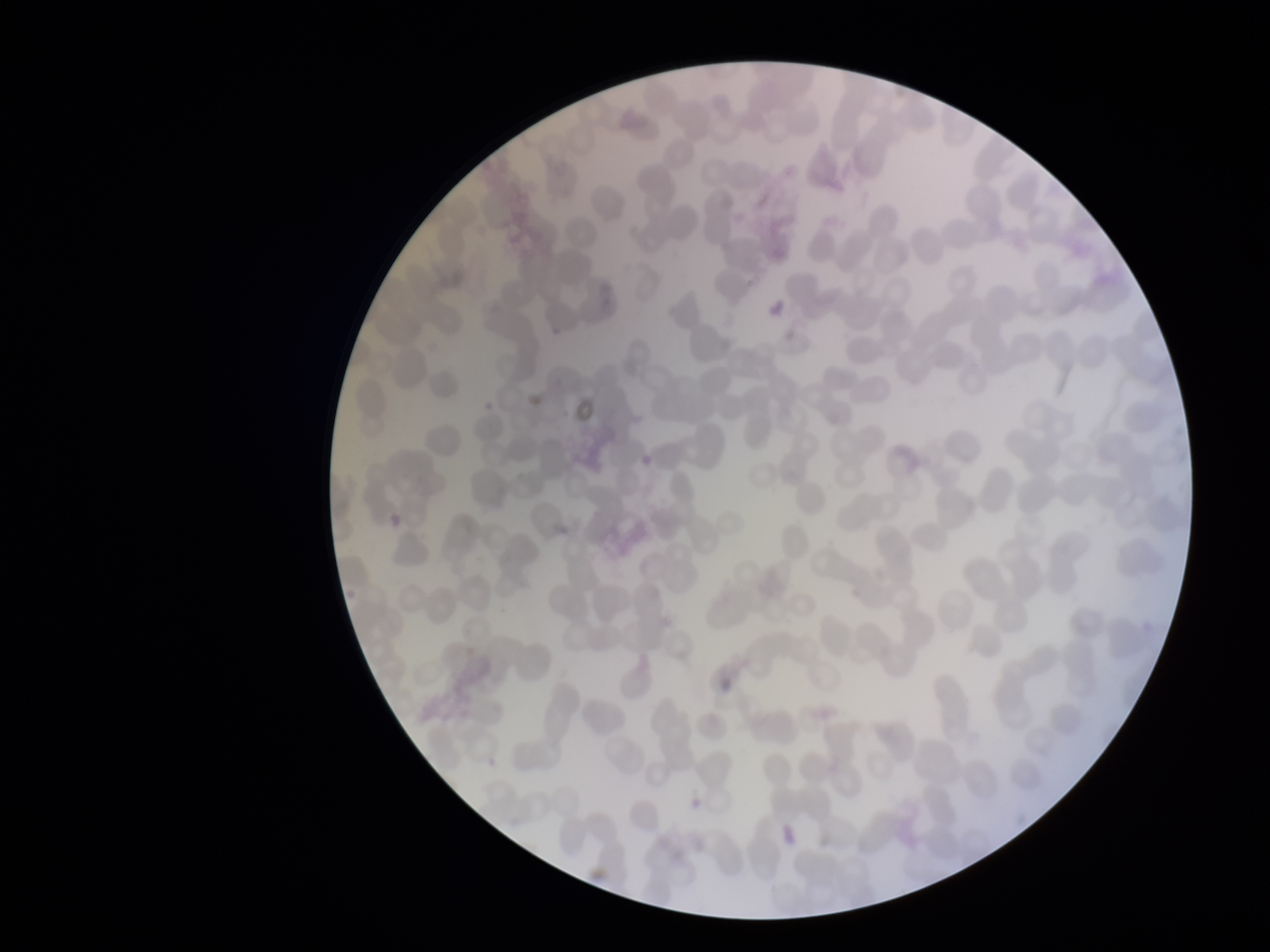

Photographed through the microscope eyepiece with a smartphone camera. Parasitized red blood cell count: 0. Stained with Giemsa. Parasitized red blood cells: none detected. Preparation: thin blood smear. Red blood cell count: 267. Patient malaria status: negative. Single field of view. Image is 1270×952 pixels.